Locate every malaria parasite.
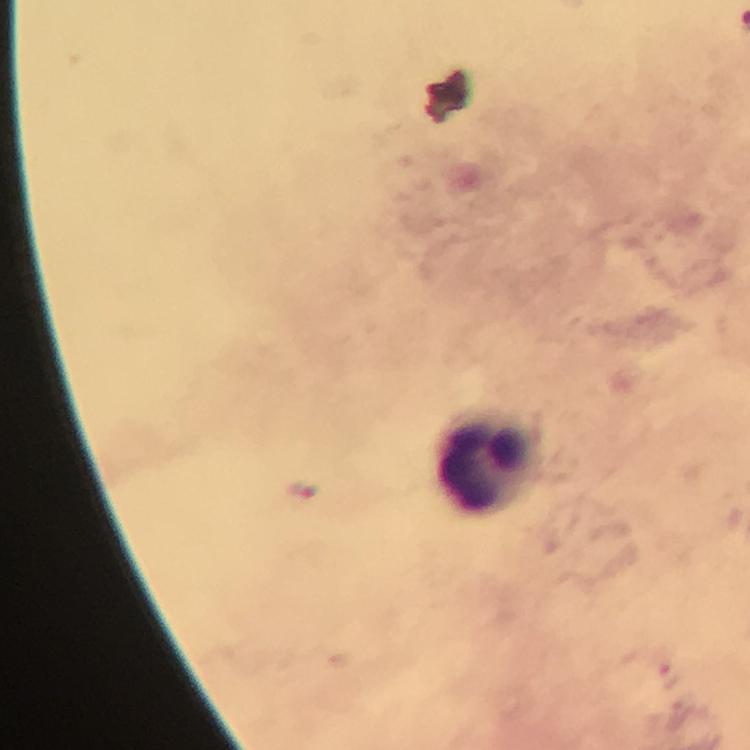
Approximate centers as (x, y) in pixels.
Malaria parasites: (300, 490).

Summary:
  - Leukocyte locations: (481, 462)
  - Context: from a diagnostic examination for malaria
  - Immersion oil: applied
  - Capture: smartphone camera through the microscope
  - Cropped from: a single field of view
  - Image size: 750×750 pixels
  - Preparation: thick blood film
  - Stain: Giemsa
  - Magnification: 100x